Assess this cell for malaria.
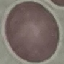

Uninfected.

{
  "stain": "Giemsa",
  "preparation": "thin smear",
  "image_type": "automatically extracted cell patch, resized to 64 × 64 pixels",
  "capture": "smartphone through the microscope eyepiece"
}